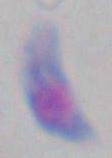

modality = photomicrograph
identification = Toxoplasma gondii
magnification = 1000x